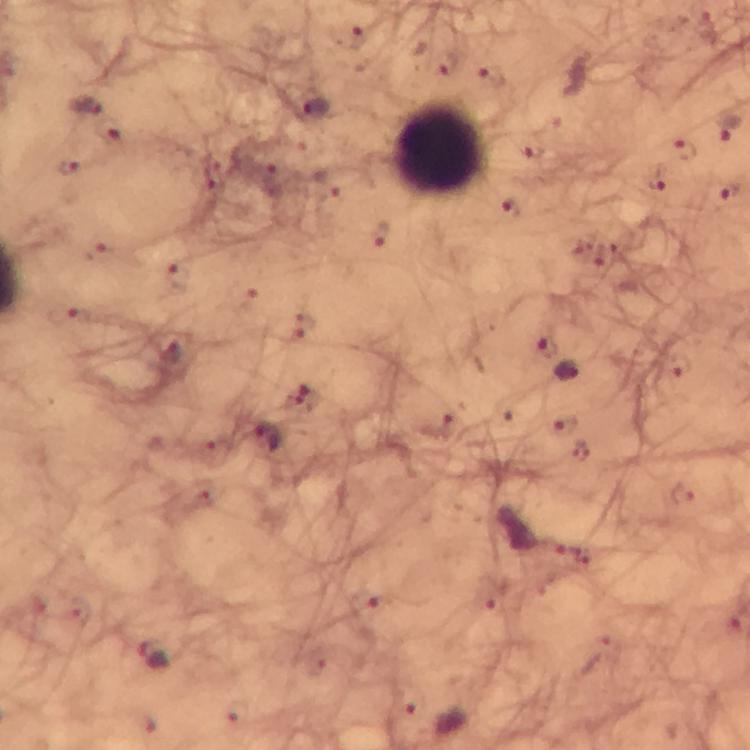

Approximate centers as (x, y) in pixels.
Summary:
  - Leukocyte locations: (442, 148)
  - Plasmodium parasite locations: (351, 38), (491, 75), (84, 106), (317, 108), (728, 127), (683, 150), (533, 151), (70, 166), (656, 183), (508, 210), (380, 235), (99, 249), (176, 274), (69, 316), (546, 345), (173, 352), (679, 365), (568, 373), (307, 397), (565, 425), (439, 426), (267, 437), (683, 494), (367, 606), (155, 655)
  - Capture: smartphone camera through the microscope
  - Magnification: 100x
  - Cropped from: one field of view
  - Preparation: thick blood film
  - Image size: 750×750 pixels
  - Stain: Giemsa
  - Immersion oil: applied
  - Context: from a malaria diagnostic workup